Point out each malaria parasite and each leukocyte.
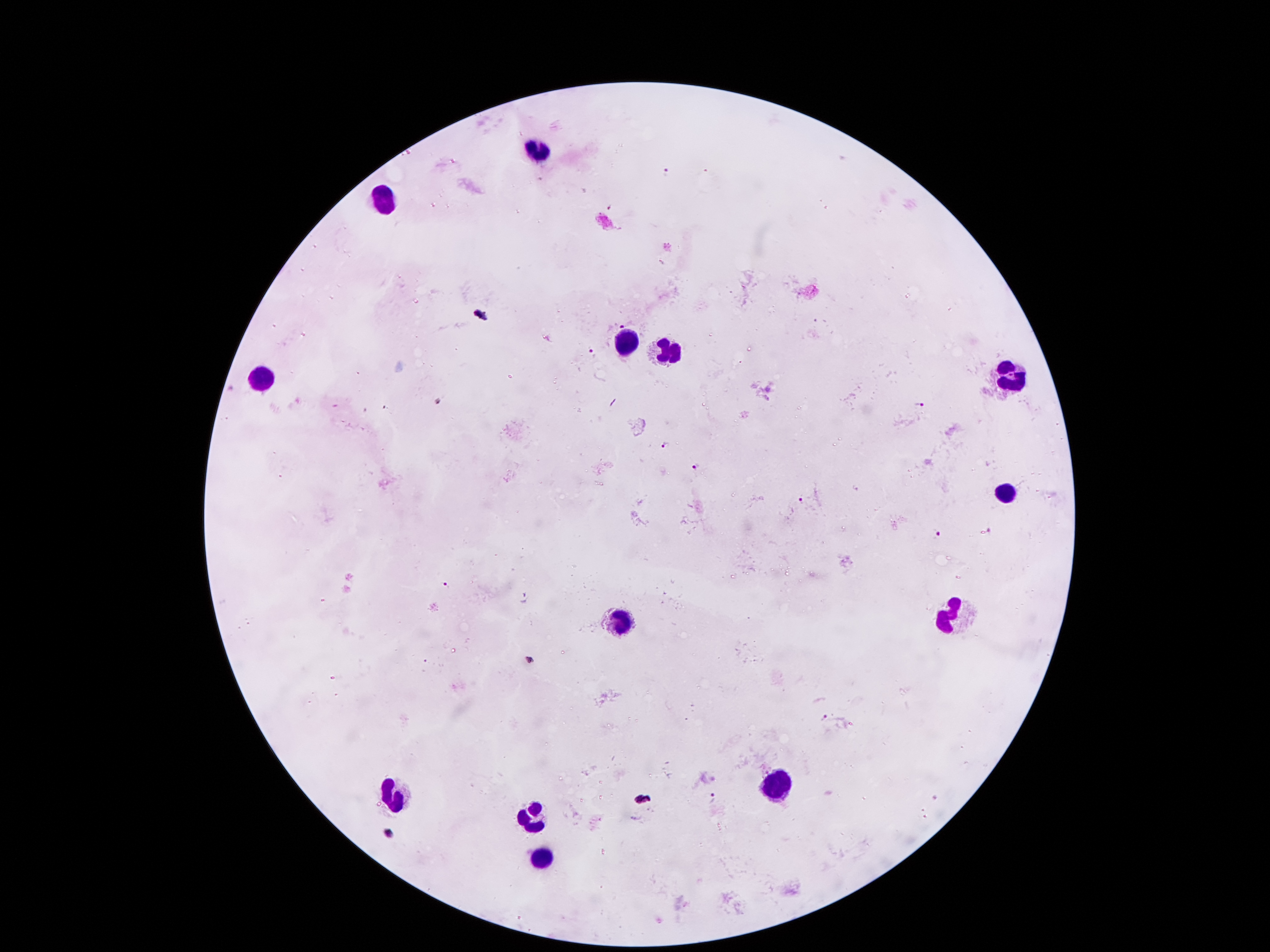
Approximate centers as [x, y] in pixels.
Malaria parasites: [667, 172], [610, 207], [480, 314], [621, 325], [591, 352], [438, 401], [920, 404], [665, 445], [695, 466], [801, 500], [990, 531], [938, 534], [445, 584], [525, 598], [529, 661], [825, 717], [714, 798], [643, 800], [389, 832].
Leukocytes: [539, 151], [384, 199], [629, 340], [671, 354], [1007, 375], [262, 378], [1003, 493], [623, 618], [957, 618], [776, 786], [396, 796], [531, 819], [541, 857].

patient_malaria_status: infected with Plasmodium falciparum
field_of_view: one from this slide
magnification: 100x
stain: Giemsa
capture: smartphone camera through the microscope eyepiece
image_size: 1270×952 pixels
preparation: thick peripheral-blood smear